Find each white blood cell.
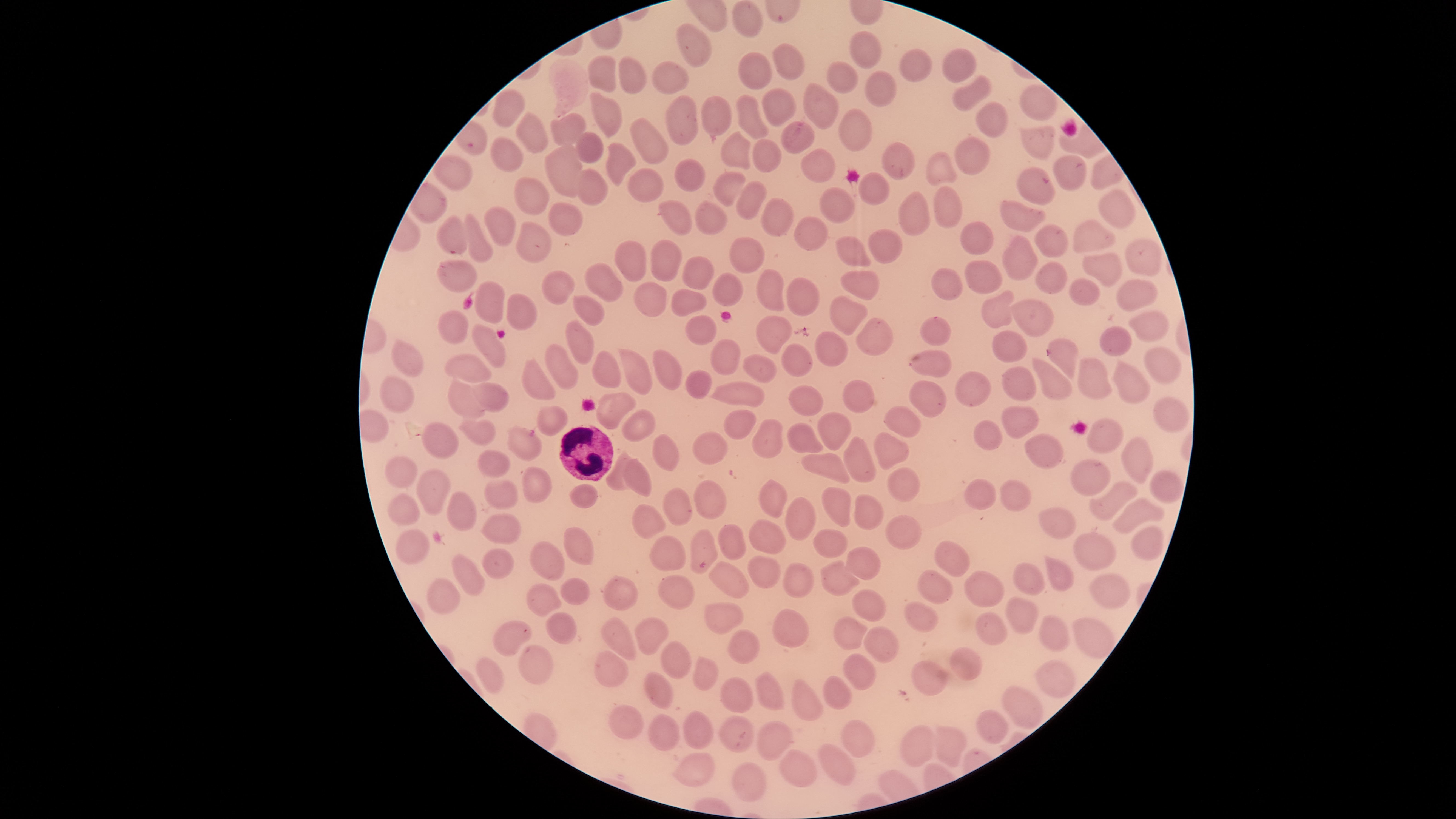
Approximate bounding boxes, in pixels from the top-left corner.
White blood cells: (left=559, top=425, right=614, bottom=481).

Approximate bounding boxes, in pixels from the top-left corner. Parasitized red blood cells: (left=437, top=215, right=471, bottom=254), (left=1047, top=338, right=1080, bottom=381). Uninfected red blood cells: (left=733, top=1, right=763, bottom=38), (left=677, top=23, right=711, bottom=67), (left=849, top=32, right=882, bottom=70), (left=772, top=43, right=804, bottom=79), (left=942, top=49, right=976, bottom=83), (left=899, top=50, right=931, bottom=83), (left=739, top=53, right=771, bottom=89), (left=589, top=54, right=618, bottom=93), (left=619, top=59, right=647, bottom=94), (left=652, top=62, right=689, bottom=94), (left=826, top=62, right=859, bottom=94), (left=865, top=72, right=896, bottom=107), (left=952, top=76, right=991, bottom=111), (left=805, top=83, right=838, bottom=129), (left=1019, top=86, right=1056, bottom=120), (left=762, top=88, right=796, bottom=126), (left=493, top=91, right=524, bottom=127), (left=590, top=92, right=621, bottom=137), (left=737, top=95, right=769, bottom=138), (left=665, top=97, right=699, bottom=146), (left=702, top=98, right=731, bottom=136), (left=974, top=102, right=1007, bottom=139), (left=838, top=108, right=871, bottom=152), (left=516, top=112, right=548, bottom=152), (left=550, top=112, right=586, bottom=147), (left=629, top=117, right=667, bottom=163), (left=780, top=121, right=816, bottom=154), (left=1020, top=126, right=1055, bottom=158), (left=721, top=132, right=750, bottom=171), (left=575, top=133, right=603, bottom=163), (left=491, top=138, right=522, bottom=172), (left=953, top=138, right=988, bottom=175), (left=753, top=140, right=782, bottom=174), (left=882, top=142, right=915, bottom=180), (left=545, top=143, right=582, bottom=198), (left=606, top=144, right=635, bottom=187), (left=801, top=148, right=837, bottom=182), (left=927, top=154, right=956, bottom=186), (left=434, top=156, right=472, bottom=191), (left=1052, top=156, right=1086, bottom=190), (left=674, top=158, right=705, bottom=192), (left=1016, top=166, right=1055, bottom=205), (left=628, top=167, right=664, bottom=202), (left=576, top=170, right=607, bottom=204), (left=713, top=171, right=745, bottom=207), (left=859, top=173, right=889, bottom=206), (left=515, top=178, right=548, bottom=214), (left=737, top=182, right=765, bottom=219), (left=932, top=184, right=962, bottom=227), (left=820, top=187, right=856, bottom=224), (left=1098, top=190, right=1135, bottom=229), (left=898, top=192, right=930, bottom=238), (left=761, top=198, right=793, bottom=237), (left=659, top=201, right=692, bottom=235), (left=1002, top=201, right=1046, bottom=231), (left=695, top=202, right=728, bottom=236), (left=548, top=203, right=581, bottom=235), (left=484, top=206, right=517, bottom=247), (left=464, top=214, right=492, bottom=261), (left=794, top=216, right=827, bottom=250), (left=1073, top=220, right=1116, bottom=252), (left=515, top=222, right=551, bottom=262), (left=960, top=222, right=992, bottom=254), (left=1035, top=225, right=1067, bottom=257), (left=866, top=226, right=903, bottom=264), (left=836, top=233, right=872, bottom=269), (left=728, top=236, right=765, bottom=274), (left=1002, top=236, right=1037, bottom=281), (left=1126, top=239, right=1163, bottom=275), (left=649, top=240, right=680, bottom=282), (left=614, top=241, right=646, bottom=282), (left=1084, top=253, right=1121, bottom=286), (left=683, top=257, right=715, bottom=291), (left=438, top=259, right=478, bottom=293), (left=965, top=261, right=1002, bottom=294), (left=585, top=262, right=622, bottom=301), (left=1034, top=263, right=1067, bottom=294), (left=932, top=268, right=963, bottom=301), (left=756, top=269, right=785, bottom=312), (left=841, top=270, right=879, bottom=300), (left=541, top=271, right=576, bottom=304), (left=713, top=273, right=742, bottom=306), (left=787, top=277, right=822, bottom=316), (left=1070, top=279, right=1099, bottom=305), (left=1117, top=279, right=1159, bottom=312), (left=474, top=280, right=505, bottom=324), (left=633, top=282, right=666, bottom=317), (left=670, top=288, right=708, bottom=316), (left=981, top=290, right=1014, bottom=327), (left=506, top=294, right=537, bottom=332), (left=573, top=295, right=604, bottom=325), (left=830, top=295, right=868, bottom=335), (left=1010, top=299, right=1054, bottom=336), (left=438, top=311, right=468, bottom=343), (left=1128, top=311, right=1169, bottom=341), (left=686, top=315, right=716, bottom=345), (left=755, top=315, right=792, bottom=356), (left=920, top=316, right=953, bottom=347), (left=566, top=317, right=595, bottom=365), (left=856, top=318, right=894, bottom=357), (left=472, top=324, right=507, bottom=368), (left=1099, top=327, right=1131, bottom=357), (left=815, top=331, right=848, bottom=365), (left=993, top=331, right=1027, bottom=363), (left=711, top=339, right=741, bottom=375), (left=391, top=340, right=422, bottom=377), (left=545, top=342, right=578, bottom=389), (left=781, top=344, right=812, bottom=377), (left=618, top=347, right=651, bottom=393), (left=1143, top=347, right=1182, bottom=385), (left=652, top=349, right=681, bottom=389), (left=911, top=350, right=950, bottom=378), (left=593, top=351, right=619, bottom=387), (left=445, top=353, right=492, bottom=385), (left=742, top=354, right=776, bottom=382), (left=1076, top=355, right=1112, bottom=400), (left=1032, top=357, right=1070, bottom=400), (left=522, top=359, right=554, bottom=399), (left=1112, top=363, right=1149, bottom=404), (left=1001, top=365, right=1036, bottom=401), (left=687, top=370, right=711, bottom=400), (left=955, top=371, right=991, bottom=408), (left=380, top=376, right=414, bottom=412), (left=448, top=377, right=485, bottom=418), (left=842, top=380, right=874, bottom=413), (left=910, top=380, right=948, bottom=417), (left=466, top=382, right=509, bottom=411), (left=713, top=382, right=765, bottom=407), (left=789, top=385, right=823, bottom=415), (left=595, top=393, right=635, bottom=427), (left=1154, top=398, right=1188, bottom=432), (left=537, top=405, right=568, bottom=437), (left=1002, top=406, right=1040, bottom=439), (left=884, top=407, right=920, bottom=436), (left=623, top=410, right=655, bottom=441), (left=723, top=410, right=757, bottom=439), (left=817, top=413, right=851, bottom=451), (left=751, top=418, right=784, bottom=458), (left=458, top=419, right=496, bottom=446), (left=975, top=420, right=1003, bottom=450), (left=1086, top=420, right=1124, bottom=453), (left=787, top=422, right=825, bottom=455), (left=422, top=423, right=458, bottom=459), (left=508, top=426, right=541, bottom=461), (left=872, top=430, right=910, bottom=471), (left=692, top=432, right=727, bottom=464), (left=653, top=434, right=680, bottom=473), (left=1023, top=435, right=1062, bottom=467), (left=843, top=436, right=876, bottom=484), (left=1121, top=437, right=1153, bottom=483), (left=477, top=449, right=509, bottom=477), (left=802, top=452, right=851, bottom=483), (left=605, top=453, right=637, bottom=491), (left=383, top=455, right=419, bottom=489), (left=623, top=459, right=652, bottom=497), (left=1070, top=460, right=1112, bottom=498), (left=417, top=468, right=449, bottom=516), (left=522, top=468, right=552, bottom=503), (left=888, top=468, right=920, bottom=501), (left=1149, top=470, right=1183, bottom=502), (left=484, top=479, right=517, bottom=508), (left=964, top=479, right=997, bottom=511), (left=694, top=480, right=726, bottom=518), (left=759, top=480, right=787, bottom=516), (left=1000, top=481, right=1031, bottom=511), (left=1089, top=481, right=1138, bottom=521), (left=570, top=484, right=598, bottom=508), (left=664, top=487, right=692, bottom=526), (left=821, top=487, right=850, bottom=527), (left=446, top=491, right=476, bottom=532), (left=852, top=494, right=884, bottom=529), (left=387, top=495, right=418, bottom=524), (left=785, top=497, right=816, bottom=541), (left=1112, top=497, right=1165, bottom=535), (left=630, top=503, right=665, bottom=539), (left=1039, top=508, right=1075, bottom=538), (left=481, top=512, right=521, bottom=543), (left=886, top=516, right=921, bottom=550), (left=749, top=519, right=786, bottom=554), (left=718, top=523, right=746, bottom=560), (left=1130, top=525, right=1164, bottom=561), (left=564, top=528, right=594, bottom=566), (left=814, top=529, right=847, bottom=557), (left=395, top=530, right=429, bottom=564), (left=690, top=530, right=717, bottom=573), (left=1072, top=534, right=1116, bottom=570), (left=649, top=537, right=685, bottom=571), (left=933, top=540, right=969, bottom=576), (left=529, top=542, right=564, bottom=581), (left=845, top=547, right=880, bottom=579), (left=483, top=549, right=513, bottom=579), (left=749, top=554, right=781, bottom=589), (left=452, top=556, right=485, bottom=596), (left=819, top=559, right=859, bottom=596), (left=1044, top=559, right=1075, bottom=591), (left=709, top=560, right=749, bottom=599), (left=781, top=563, right=812, bottom=597), (left=1012, top=563, right=1044, bottom=595), (left=964, top=571, right=1004, bottom=606), (left=917, top=572, right=953, bottom=604), (left=1090, top=574, right=1129, bottom=608), (left=657, top=575, right=693, bottom=608), (left=604, top=577, right=637, bottom=610), (left=561, top=578, right=589, bottom=605), (left=426, top=579, right=460, bottom=615), (left=526, top=584, right=560, bottom=617), (left=852, top=588, right=887, bottom=621), (left=1005, top=598, right=1039, bottom=633), (left=705, top=602, right=743, bottom=634), (left=903, top=602, right=936, bottom=632), (left=772, top=609, right=808, bottom=651), (left=975, top=612, right=1006, bottom=645), (left=547, top=613, right=576, bottom=644), (left=831, top=616, right=871, bottom=650), (left=1041, top=616, right=1069, bottom=650), (left=599, top=617, right=637, bottom=661), (left=1073, top=618, right=1113, bottom=658), (left=635, top=619, right=669, bottom=656), (left=493, top=620, right=532, bottom=656), (left=863, top=627, right=900, bottom=662), (left=727, top=630, right=759, bottom=664), (left=660, top=642, right=691, bottom=679), (left=518, top=647, right=554, bottom=685), (left=950, top=648, right=981, bottom=681), (left=595, top=651, right=628, bottom=688), (left=843, top=654, right=876, bottom=691), (left=477, top=658, right=503, bottom=694), (left=692, top=658, right=718, bottom=692), (left=912, top=662, right=946, bottom=696), (left=1036, top=662, right=1075, bottom=697), (left=644, top=672, right=672, bottom=709), (left=752, top=672, right=783, bottom=710), (left=822, top=676, right=853, bottom=710), (left=721, top=678, right=753, bottom=712), (left=791, top=680, right=822, bottom=720), (left=1002, top=686, right=1042, bottom=728), (left=609, top=705, right=643, bottom=742), (left=975, top=709, right=1008, bottom=744), (left=684, top=711, right=713, bottom=748), (left=649, top=715, right=679, bottom=750), (left=719, top=717, right=752, bottom=753), (left=842, top=720, right=875, bottom=757), (left=757, top=722, right=791, bottom=760), (left=934, top=725, right=965, bottom=768), (left=900, top=726, right=936, bottom=767), (left=819, top=746, right=854, bottom=785), (left=780, top=750, right=816, bottom=787), (left=677, top=753, right=714, bottom=787), (left=731, top=763, right=765, bottom=801). Species: Plasmodium falciparum. Photographed with a smartphone camera through the microscope eyepiece. The visible region is circular. Thin blood film. Giemsa stain. Image is 1456×819 pixels. Presence: malaria parasites identified. Single field of view.